Name the parasite shown.
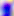
This is Toxoplasma gondii.

Micrograph. Captured at 400x magnification.